Describe the morphology of the erythrocytes.
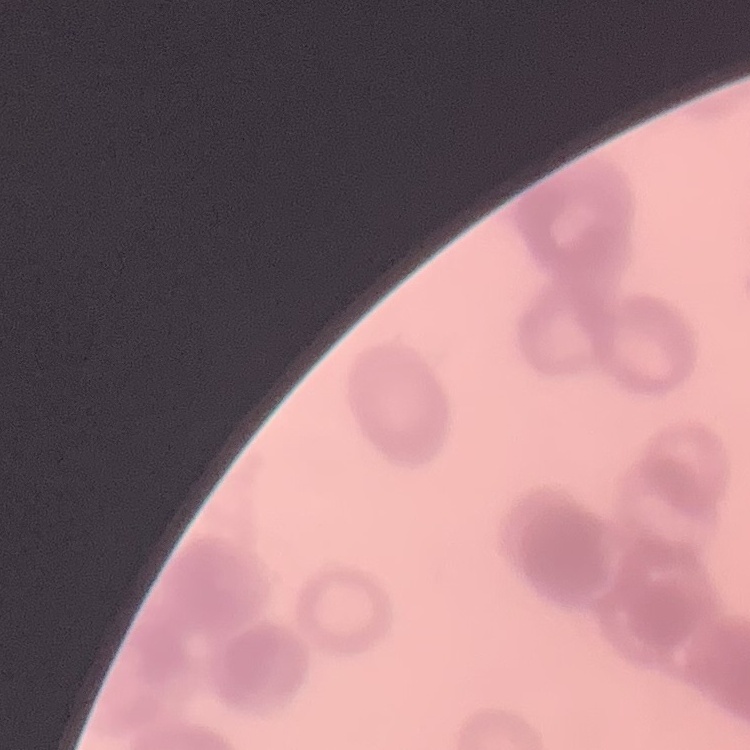

They show rouleaux formation.

Summary:
  - Image type: square crop of a larger photomicrograph
  - Stain: Field's or Giemsa
  - Preparation: thin blood smear